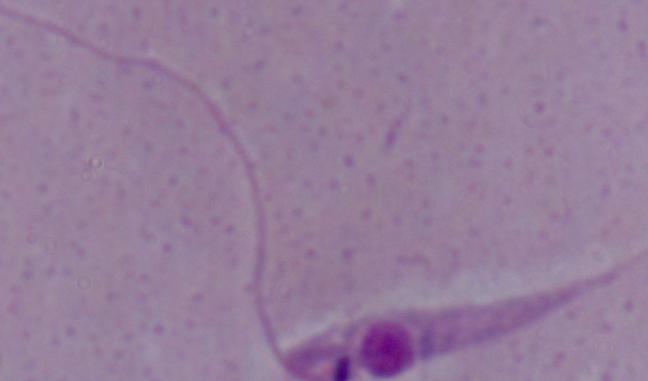
identification = Leishmania
magnification = 1000x
modality = micrograph